Report the malaria status of this cell.
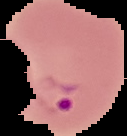
It is parasitized.

image type = segmented cell region on a black background
preparation = thin blood smear
image size = 127×136 pixels